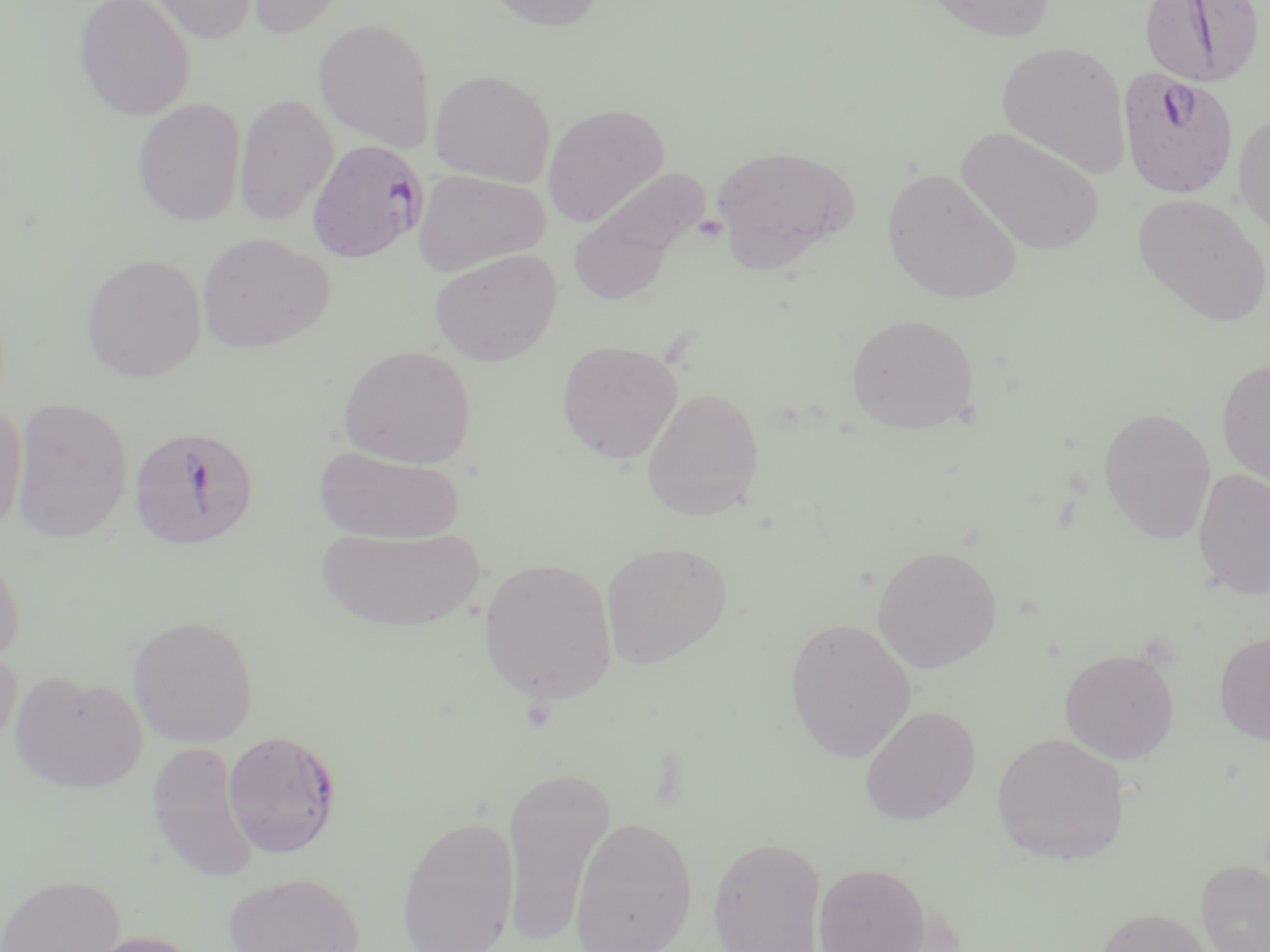

Summary:
  - Coordinate format: approximate bounding boxes as [x1, y1, x2, y2] in pixels
  - Uninfected red blood cell locations: [73, 0, 196, 120], [139, 0, 259, 44], [241, 0, 350, 38], [485, 0, 606, 32], [922, 0, 1055, 42], [314, 17, 437, 150], [996, 40, 1131, 178], [429, 69, 555, 186], [234, 93, 337, 228], [133, 97, 247, 227], [542, 104, 669, 227], [1233, 112, 1270, 235], [957, 127, 1105, 256], [711, 145, 859, 272], [882, 168, 1022, 304], [413, 170, 550, 277], [566, 170, 706, 309], [1132, 193, 1269, 326], [196, 233, 333, 354], [429, 248, 562, 366], [81, 252, 207, 383], [846, 313, 979, 434], [556, 338, 683, 464], [338, 345, 477, 469], [1217, 358, 1270, 488], [641, 385, 764, 521], [10, 396, 133, 543], [0, 403, 27, 537], [1098, 407, 1217, 544], [314, 445, 465, 545], [1193, 468, 1270, 600], [315, 525, 487, 632], [600, 540, 733, 669], [0, 544, 26, 670], [872, 545, 1002, 673], [478, 557, 618, 706], [127, 614, 259, 747], [784, 617, 916, 763], [1214, 631, 1270, 745], [0, 645, 22, 755], [1059, 647, 1180, 764], [9, 671, 148, 794], [859, 705, 981, 825], [991, 731, 1129, 865], [145, 740, 260, 885], [501, 765, 615, 944], [397, 813, 520, 952], [569, 816, 698, 952], [707, 836, 827, 952], [1197, 859, 1270, 952], [812, 861, 932, 952], [223, 872, 364, 952], [0, 873, 125, 952], [1095, 907, 1216, 952], [74, 929, 208, 952]
  - Plasmodium falciparum-infected red blood cell locations: [1139, 0, 1266, 89], [1117, 67, 1239, 199], [307, 139, 429, 262], [129, 424, 260, 550], [223, 729, 341, 859]
  - Slide-level diagnosis: Plasmodium falciparum
  - Field of view: one of a larger specimen
  - Stain: May-Grünwald-Giemsa
  - Image size: 1270×952 pixels
  - Preparation: thin blood film
  - Modality: light microscopy
  - Magnification: 1000x